Assess this cell for malaria.
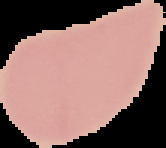
Uninfected.

Segmented cell region on a black background. Image is 166×148 pixels. From a thin blood film.